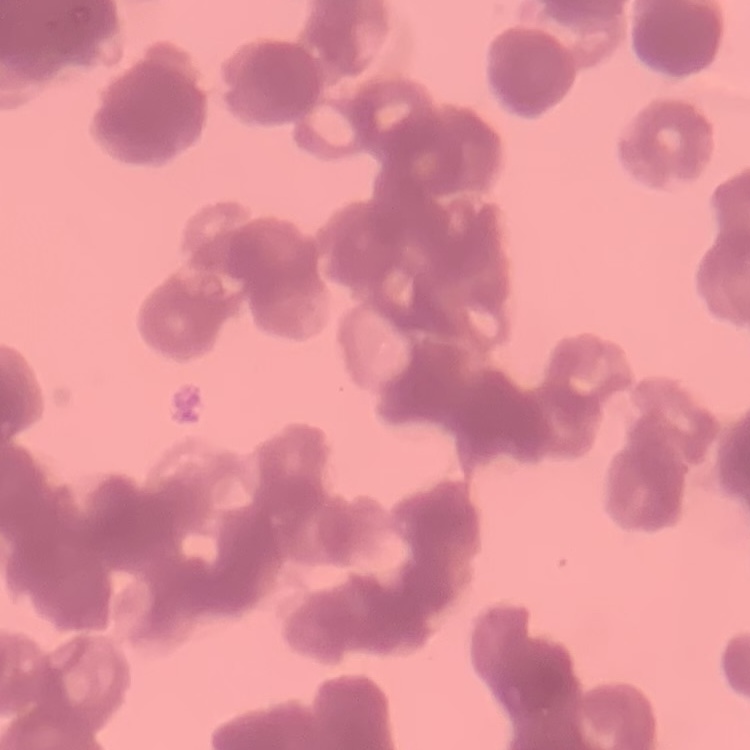

red_blood_cell_morphology: rouleaux formation
preparation: thin blood smear
image_type: one tile cut from a larger photomicrograph
stain: Field's or Giemsa